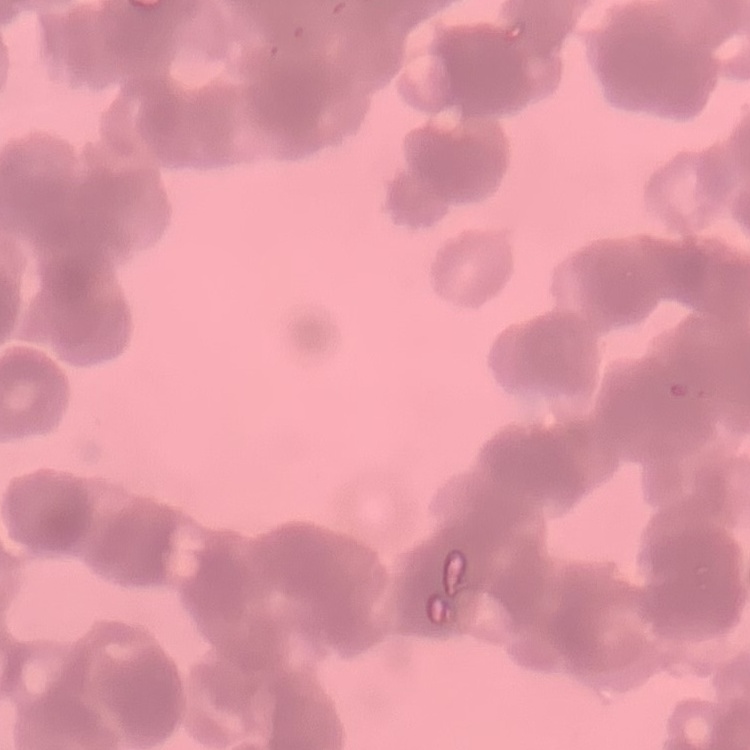 The red blood cells show rouleaux formation. Stained with either Field's or Giemsa. Square crop of a larger photomicrograph. Thin peripheral smear.